State the blood parasite species.
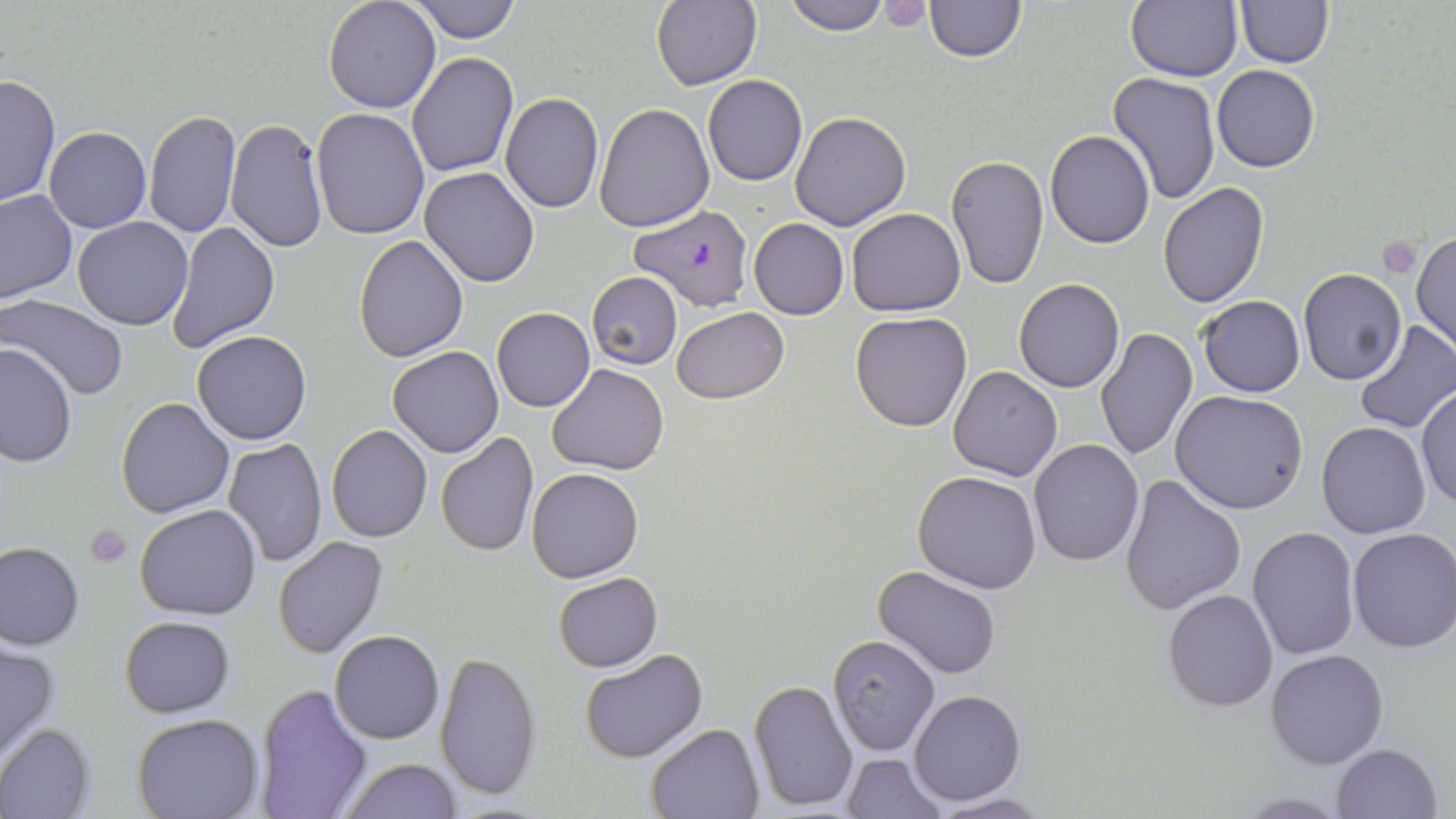
Plasmodium falciparum.

Summary:
  - Coordinate format: approximate bounding boxes as [x1, y1, x2, y2] in pixels
  - Platelet locations: [1376, 237, 1424, 279], [85, 524, 132, 567]
  - Plasmodium falciparum-infected red blood cell locations: [631, 203, 755, 312]
  - Uninfected red blood cell locations: [322, 0, 442, 113], [783, 0, 890, 35], [871, 0, 940, 30], [924, 0, 1025, 62], [1125, 0, 1243, 82], [407, 1, 524, 44], [651, 1, 761, 89], [1235, 1, 1333, 68], [407, 53, 518, 177], [1212, 64, 1320, 172], [1108, 72, 1222, 204], [0, 75, 60, 209], [701, 75, 808, 186], [501, 93, 604, 212], [593, 101, 713, 232], [312, 108, 430, 240], [144, 110, 240, 240], [789, 111, 911, 229], [226, 118, 328, 253], [43, 127, 152, 233], [1044, 129, 1155, 247], [947, 154, 1048, 289], [420, 166, 540, 287], [1156, 182, 1269, 306], [0, 190, 76, 304], [846, 207, 965, 315], [72, 216, 195, 330], [748, 217, 848, 320], [167, 222, 280, 354], [1413, 228, 1455, 355], [353, 235, 469, 361], [1298, 268, 1406, 383], [587, 272, 683, 370], [1013, 279, 1124, 392], [1, 294, 131, 401], [1197, 294, 1305, 397], [672, 306, 787, 403], [491, 308, 595, 412], [850, 311, 971, 433], [1353, 323, 1456, 436], [1095, 328, 1197, 461], [190, 331, 311, 445], [408, 343, 519, 552], [1, 345, 76, 466], [389, 346, 503, 458], [548, 363, 669, 475], [949, 365, 1061, 481], [1416, 384, 1456, 512], [1171, 390, 1310, 514], [116, 397, 235, 519], [1317, 421, 1432, 539], [327, 425, 432, 542], [434, 431, 538, 557], [222, 438, 328, 567], [1028, 439, 1144, 567], [527, 466, 644, 584], [912, 471, 1042, 594], [1119, 472, 1246, 616], [135, 504, 263, 620], [1246, 527, 1361, 662], [1346, 528, 1456, 653], [273, 536, 388, 659], [0, 541, 84, 649], [875, 566, 1002, 678], [553, 572, 662, 672], [851, 587, 969, 736], [1163, 589, 1279, 712], [120, 616, 234, 716], [330, 629, 444, 744], [827, 635, 940, 756], [0, 640, 60, 763], [1265, 647, 1390, 769], [580, 648, 708, 764], [434, 650, 540, 801], [750, 677, 857, 811], [255, 683, 372, 818], [909, 690, 1026, 807], [134, 713, 262, 819], [646, 722, 764, 817], [0, 724, 94, 819], [1331, 743, 1443, 819], [843, 753, 945, 819], [339, 758, 463, 818], [1233, 792, 1350, 817], [927, 793, 1053, 818]
  - Magnification: 1000x
  - Modality: optical microscopy
  - Field of view: one of a larger specimen
  - Preparation: thin blood smear
  - Stain: May-Grünwald-Giemsa
  - Image size: 1456×819 pixels